Assess this cell for malaria.
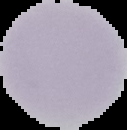
It is uninfected.

image type = segmented cell region with the area outside set to black
preparation = thin blood smear
image size = 127×130 pixels